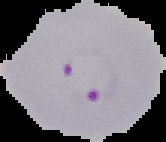
{
  "result": "malaria parasites identified",
  "image_size": "166×142 pixels",
  "image_type": "segmented cell region on a black background",
  "preparation": "thin blood film"
}